Classify this cell by malaria status.
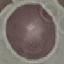

It is uninfected.

capture: smartphone through the microscope eyepiece
stain: Giemsa
image_type: automatically extracted cell patch, resized to 64 × 64 pixels
preparation: thin blood film